Describe the morphology of the erythrocytes.
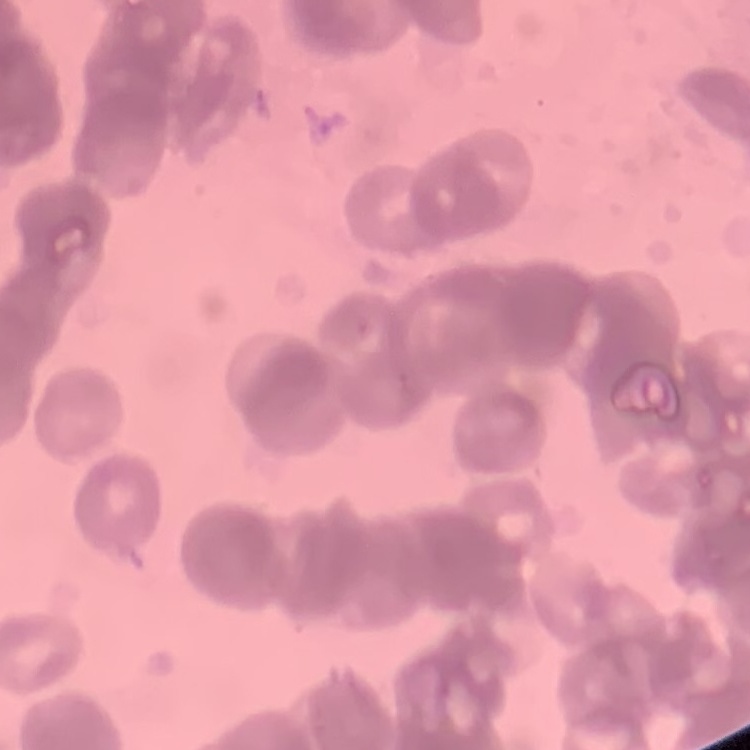
Rouleaux formation.

Summary:
  - Image type: square crop of a larger photomicrograph
  - Stain: Field's or Giemsa
  - Preparation: thin blood film